Identify the parasite.
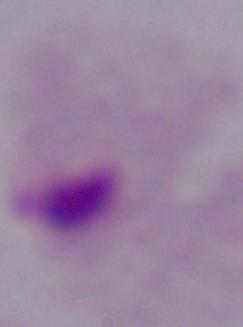

A trichomonad.

Micrograph. Captured at 1000x magnification.